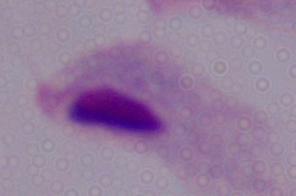

A trichomonad is seen. 1000x magnification. Photomicrograph.